Point out each Plasmodium parasite.
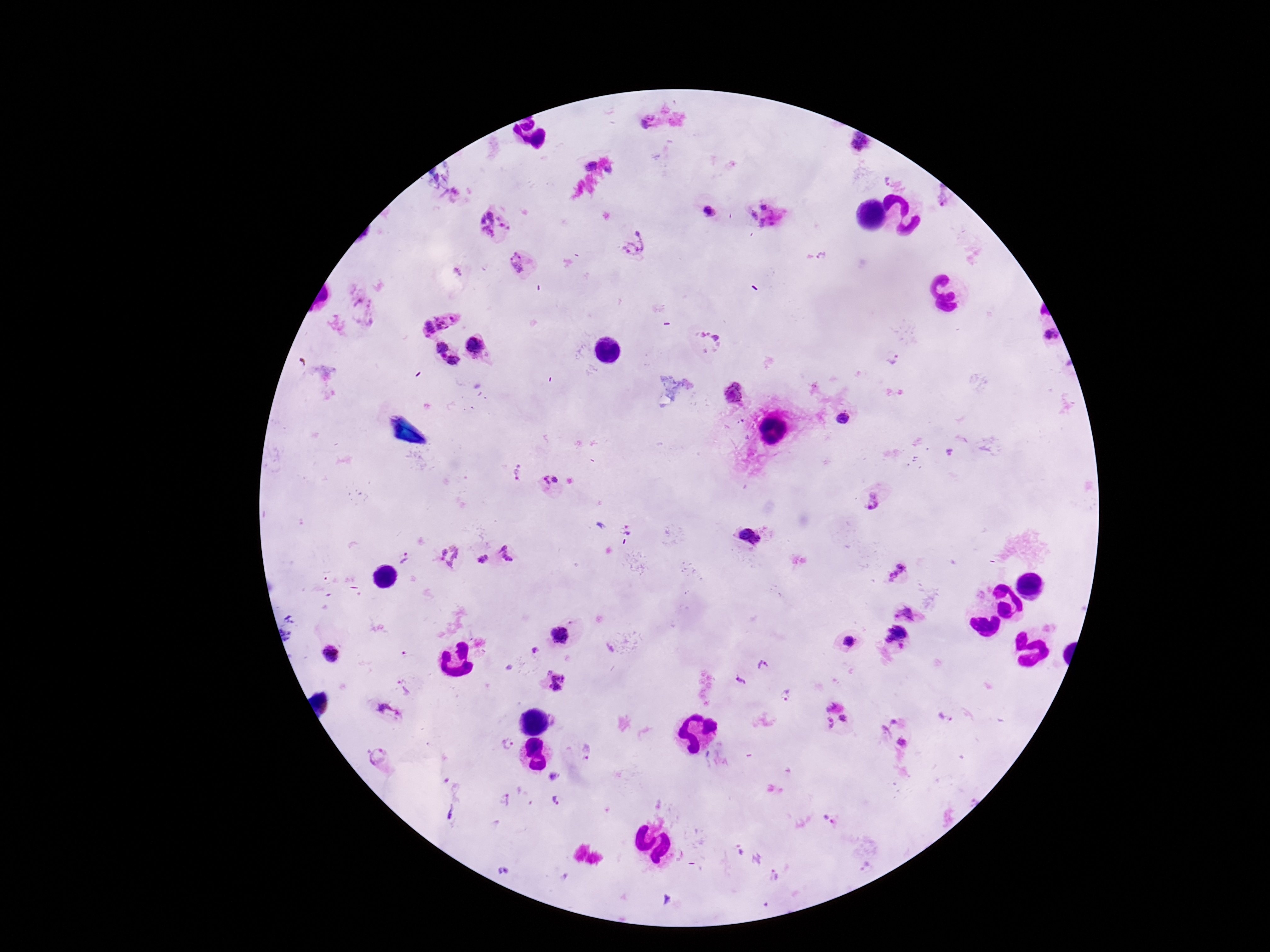

Approximate centers as (x, y) in pixels.
Plasmodium parasites: (649, 122), (857, 145), (588, 164), (888, 182), (709, 209), (767, 215), (491, 224), (634, 242), (517, 263), (435, 315), (1048, 337), (706, 341), (476, 345), (440, 348), (894, 359), (452, 361), (733, 394), (843, 419), (518, 475), (552, 485), (873, 506), (626, 530), (751, 536), (447, 557), (407, 559), (509, 559), (478, 561), (898, 570), (906, 612), (896, 634), (559, 637), (847, 640), (534, 651), (333, 656), (762, 665), (741, 680), (408, 682), (557, 685), (786, 695), (830, 705), (386, 713), (844, 717), (830, 723), (903, 744), (506, 746), (584, 748), (379, 756), (552, 778), (555, 798), (505, 801), (451, 815), (829, 821).

Summary:
  - Image size: 1270×952 pixels
  - Patient malaria status: infected
  - Magnification: 100x
  - Capture: smartphone camera through the microscope eyepiece
  - Field of view: one from this slide
  - Preparation: thick blood film
  - Stain: Giemsa